Assess for Plasmodium parasites.
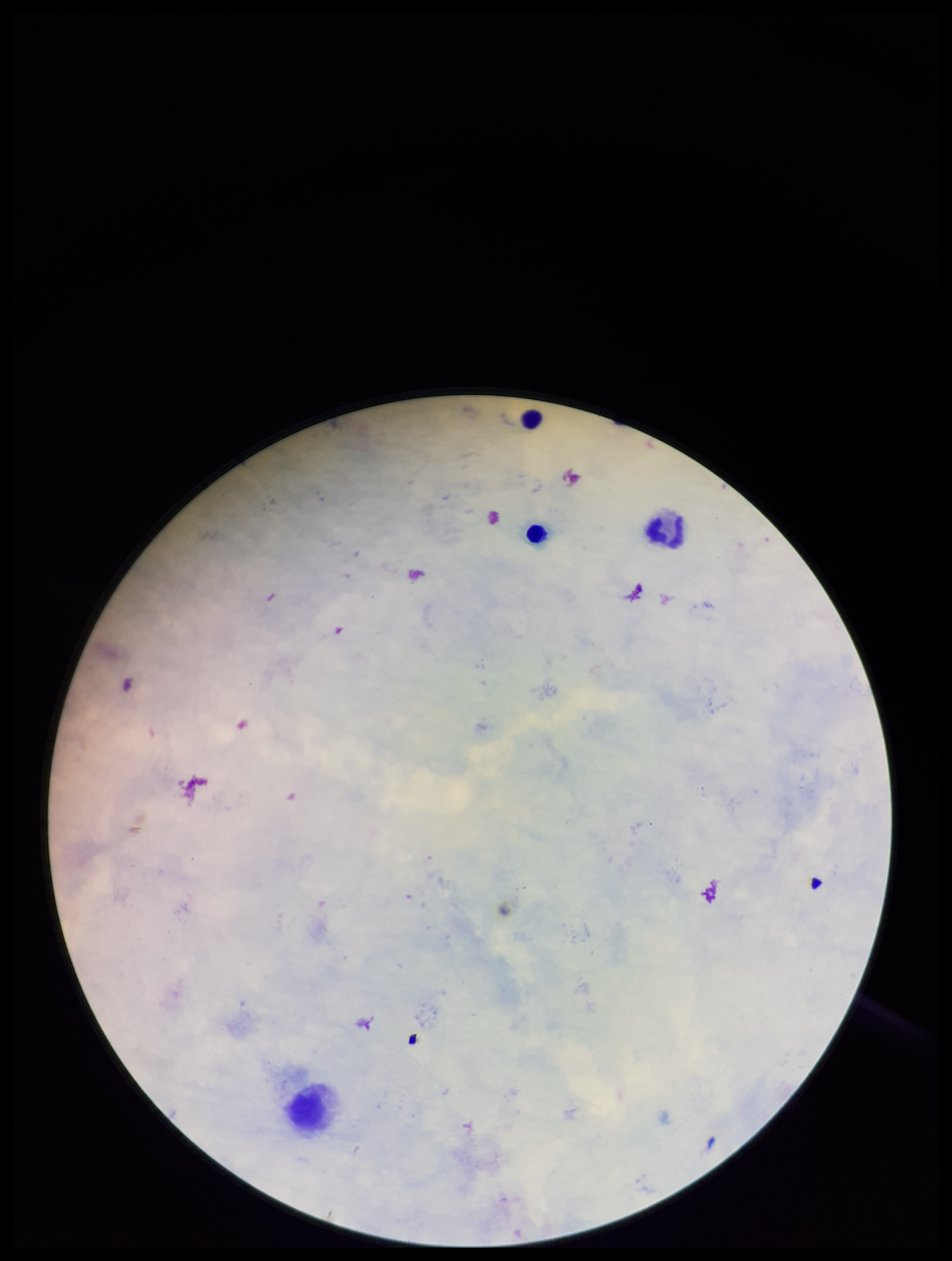

None seen.

stain = Giemsa
preparation = thick blood smear
leukocyte count = 3
patient malaria status = negative
capture = smartphone photograph through the microscope eyepiece
image size = 952×1261 pixels
parasite count = 0
field of view = one from this slide